Locate every Plasmodium vivax-infected red blood cell.
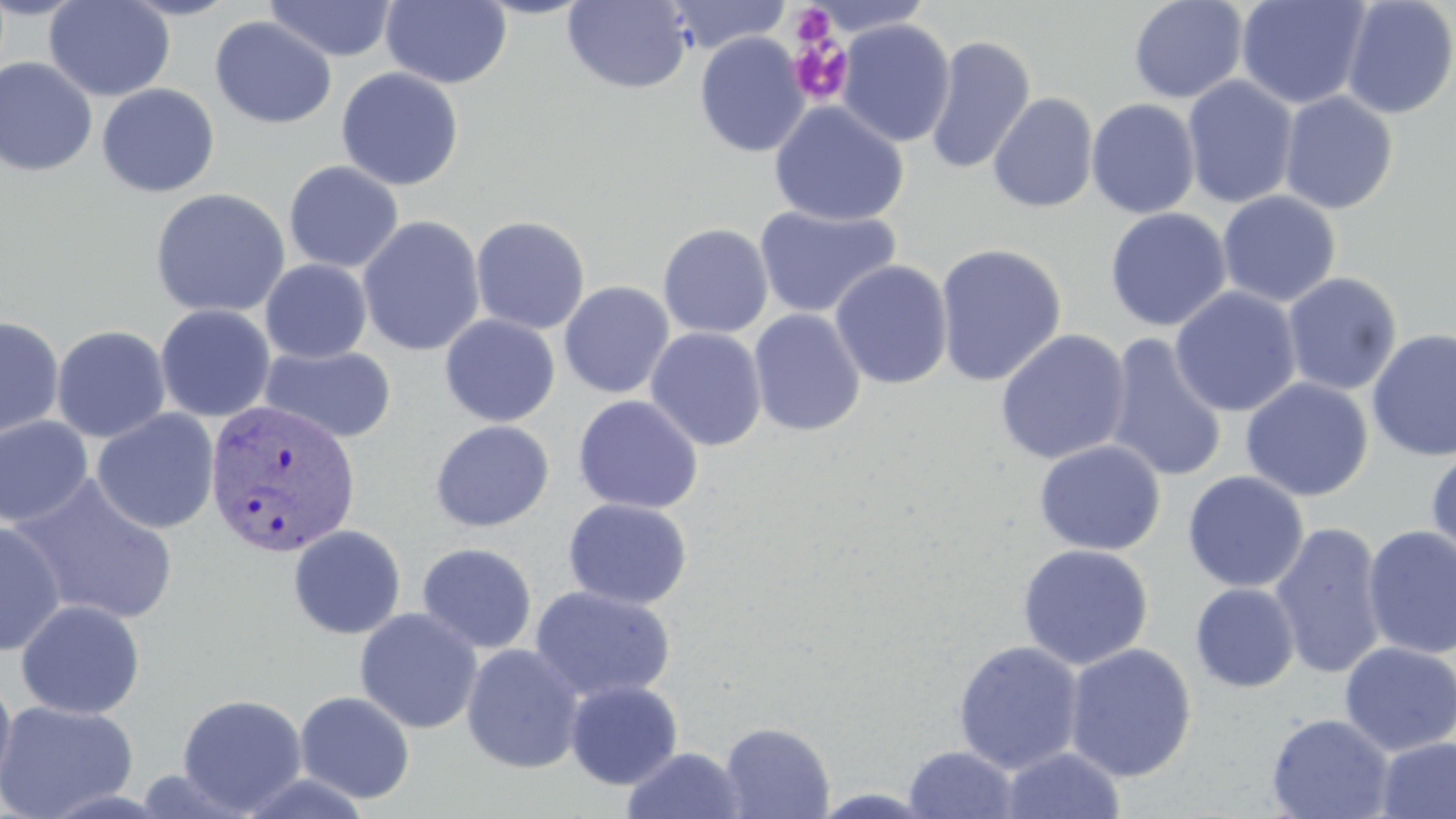

Approximate bounding boxes as (x1,y1)-(x2,y2) corner pairs in pixels.
Plasmodium vivax-infected red blood cells: (203,398)-(361,559).

Summary:
  - Platelet locations: (790,5)-(837,48), (788,37)-(853,105)
  - Uninfected red blood cell locations: (44,0)-(175,102), (117,0)-(242,21), (380,0)-(512,89), (472,0)-(597,19), (562,0)-(692,93), (664,0)-(790,54), (1128,0)-(1249,104), (1236,0)-(1373,110), (264,1)-(397,62), (1340,1)-(1456,119), (209,16)-(338,130), (837,19)-(955,148), (694,31)-(810,158), (924,35)-(1036,175), (0,57)-(98,177), (336,67)-(465,191), (1182,75)-(1299,209), (96,83)-(221,197), (1279,91)-(1399,214), (987,92)-(1099,213), (1086,98)-(1201,219), (769,100)-(909,227), (283,161)-(404,273), (150,187)-(291,318), (1217,191)-(1340,307), (753,205)-(903,319), (1104,207)-(1232,332), (357,215)-(485,357), (470,215)-(591,335), (657,223)-(774,339), (934,242)-(1068,387), (260,259)-(373,363), (829,260)-(953,390), (1281,272)-(1402,396), (558,281)-(675,399), (1169,286)-(1302,417), (155,304)-(276,422), (748,308)-(866,437), (439,314)-(560,427), (0,317)-(65,441), (51,325)-(172,443), (645,327)-(767,451), (1366,328)-(1456,462), (995,329)-(1132,466), (1104,333)-(1228,484), (259,344)-(397,444), (1240,377)-(1374,501), (572,395)-(704,514), (91,409)-(220,535), (0,415)-(95,529), (429,419)-(555,533), (1034,440)-(1165,556), (1425,448)-(1456,569), (1182,471)-(1309,593), (9,473)-(180,626), (563,498)-(692,610), (0,520)-(66,657), (1269,520)-(1388,680), (287,524)-(407,640), (1362,525)-(1456,660), (417,543)-(538,654), (1016,543)-(1154,670), (1190,583)-(1300,693), (528,585)-(677,703), (15,599)-(146,719), (354,607)-(483,734), (952,640)-(1084,774), (1339,642)-(1456,756), (461,643)-(585,774), (1063,643)-(1197,782), (0,669)-(17,804), (564,679)-(683,790), (294,691)-(416,804), (177,694)-(308,815), (0,700)-(139,819), (1266,713)-(1394,819), (719,721)-(835,819), (1374,736)-(1456,819), (903,745)-(1021,818), (621,746)-(748,819), (999,746)-(1127,819)
  - Slide-level diagnosis: Plasmodium vivax
  - Preparation: thin blood smear
  - Field of view: single
  - Magnification: 1000x
  - Modality: light microscopy
  - Stain: May-Grünwald-Giemsa
  - Image size: 1456×819 pixels